Classify this cell by malaria status.
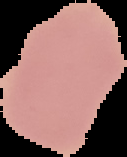
It is uninfected.

Image is 127×157 pixels. From a thin blood smear. Segmented cell region on a black background.